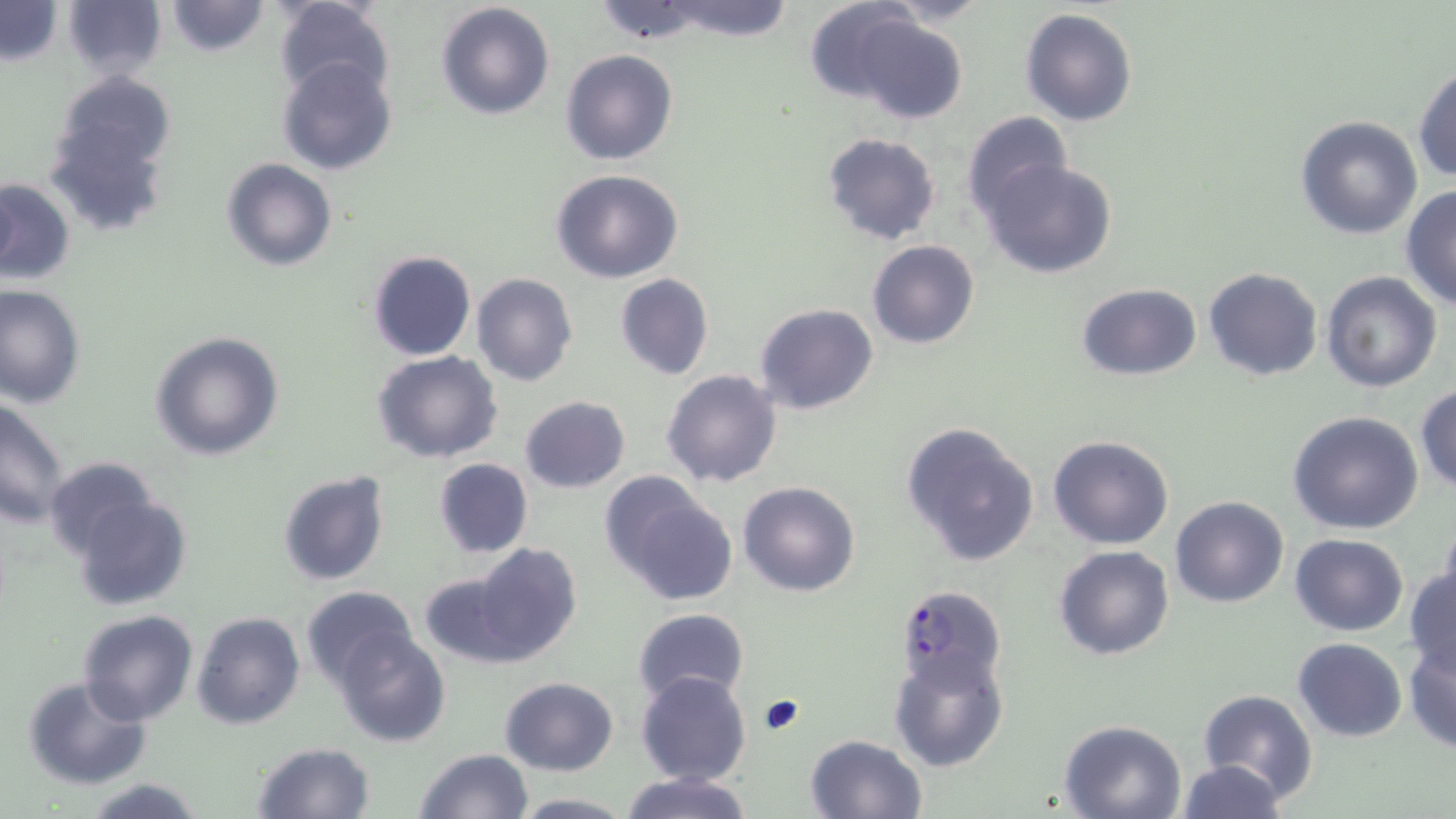
slide_level_diagnosis: Plasmodium falciparum
field_of_view: one of a larger specimen
preparation: thin blood film
plasmodium_falciparum_infected_red_blood_cell_locations: 'approximate bounding boxes as named x1/y1/x2/y2 corners in pixels: (x1=895, y1=584, x2=1009, y2=691)'
image_size: 1456×819 pixels
modality: light microscopy
stain: May-Grünwald-Giemsa
magnification: 1000x
uninfected_red_blood_cell_locations: 'approximate bounding boxes as named x1/y1/x2/y2 corners in pixels: (x1=274, y1=0, x2=397, y2=108), (x1=660, y1=0, x2=796, y2=40), (x1=803, y1=0, x2=920, y2=101), (x1=876, y1=0, x2=993, y2=27), (x1=0, y1=1, x2=64, y2=68), (x1=61, y1=1, x2=166, y2=80), (x1=165, y1=1, x2=270, y2=57), (x1=434, y1=2, x2=555, y2=120), (x1=1020, y1=9, x2=1138, y2=128), (x1=849, y1=16, x2=969, y2=125), (x1=560, y1=48, x2=678, y2=166), (x1=276, y1=56, x2=400, y2=176), (x1=1412, y1=64, x2=1456, y2=184), (x1=54, y1=71, x2=176, y2=175), (x1=46, y1=111, x2=171, y2=237), (x1=960, y1=112, x2=1075, y2=220), (x1=1295, y1=116, x2=1423, y2=240), (x1=822, y1=132, x2=941, y2=245), (x1=222, y1=158, x2=337, y2=272), (x1=980, y1=158, x2=1119, y2=279), (x1=550, y1=168, x2=685, y2=284), (x1=0, y1=177, x2=76, y2=287), (x1=1400, y1=186, x2=1456, y2=309), (x1=867, y1=239, x2=980, y2=350), (x1=367, y1=250, x2=476, y2=361), (x1=365, y1=265, x2=576, y2=378), (x1=1203, y1=267, x2=1323, y2=382), (x1=1320, y1=271, x2=1442, y2=392), (x1=471, y1=273, x2=578, y2=387), (x1=615, y1=273, x2=714, y2=380), (x1=1077, y1=283, x2=1202, y2=380), (x1=1, y1=285, x2=86, y2=406), (x1=755, y1=303, x2=877, y2=415), (x1=150, y1=331, x2=286, y2=462), (x1=371, y1=350, x2=503, y2=463), (x1=662, y1=369, x2=783, y2=490), (x1=1415, y1=383, x2=1456, y2=491), (x1=519, y1=395, x2=630, y2=493), (x1=0, y1=396, x2=70, y2=527), (x1=1287, y1=411, x2=1425, y2=535), (x1=900, y1=420, x2=1041, y2=567), (x1=1048, y1=434, x2=1175, y2=550), (x1=42, y1=456, x2=160, y2=560), (x1=433, y1=458, x2=533, y2=558), (x1=277, y1=470, x2=391, y2=588), (x1=601, y1=475, x2=733, y2=602), (x1=737, y1=481, x2=860, y2=598), (x1=72, y1=492, x2=192, y2=611), (x1=1170, y1=495, x2=1288, y2=607), (x1=1440, y1=515, x2=1456, y2=611), (x1=1289, y1=534, x2=1410, y2=637), (x1=471, y1=543, x2=584, y2=664), (x1=1053, y1=545, x2=1176, y2=661), (x1=1404, y1=566, x2=1456, y2=677), (x1=418, y1=574, x2=523, y2=667), (x1=301, y1=586, x2=415, y2=686), (x1=632, y1=608, x2=749, y2=708), (x1=76, y1=610, x2=199, y2=727), (x1=192, y1=611, x2=306, y2=730), (x1=332, y1=629, x2=451, y2=747), (x1=1292, y1=637, x2=1407, y2=742), (x1=1403, y1=640, x2=1455, y2=754), (x1=888, y1=646, x2=1009, y2=772), (x1=636, y1=670, x2=751, y2=785), (x1=22, y1=675, x2=152, y2=790), (x1=499, y1=676, x2=618, y2=776), (x1=1197, y1=689, x2=1320, y2=806), (x1=1058, y1=718, x2=1188, y2=817), (x1=803, y1=734, x2=928, y2=818), (x1=250, y1=741, x2=375, y2=818), (x1=412, y1=748, x2=532, y2=819), (x1=1175, y1=759, x2=1287, y2=818), (x1=619, y1=771, x2=753, y2=819), (x1=77, y1=777, x2=209, y2=819), (x1=512, y1=793, x2=636, y2=817)'